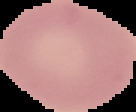
From a thin blood film. Image is 136×112 pixels. Malaria status: uninfected. Cell region segmented out of the field of view; the surrounding area is masked to black.